Classify this cell by malaria status.
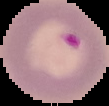

Parasitized.

From a thin blood smear. Image is 109×106 pixels. The area outside the segmented cell region is set to black.